Assess the morphology of the red blood cells.
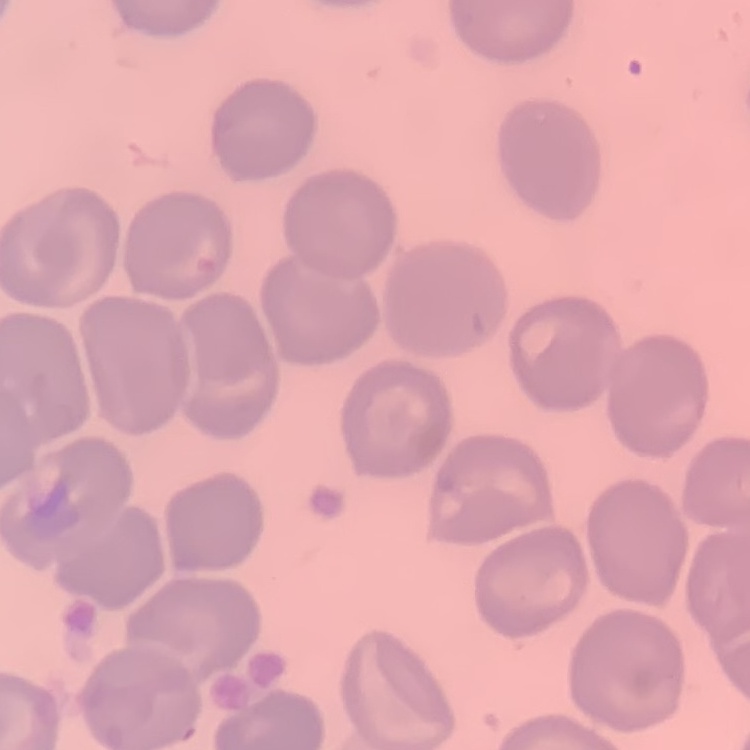

No rouleaux formation.

Summary:
  - Stain: Field's or Giemsa
  - Image type: square crop of a larger photomicrograph
  - Preparation: thin peripheral smear